Assess this cell for malaria.
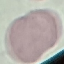

It is uninfected.

Summary:
  - Stain: Giemsa
  - Image type: automatically extracted cell patch, resized to 64 × 64 pixels
  - Preparation: thin blood smear
  - Capture: smartphone camera at the microscope eyepiece